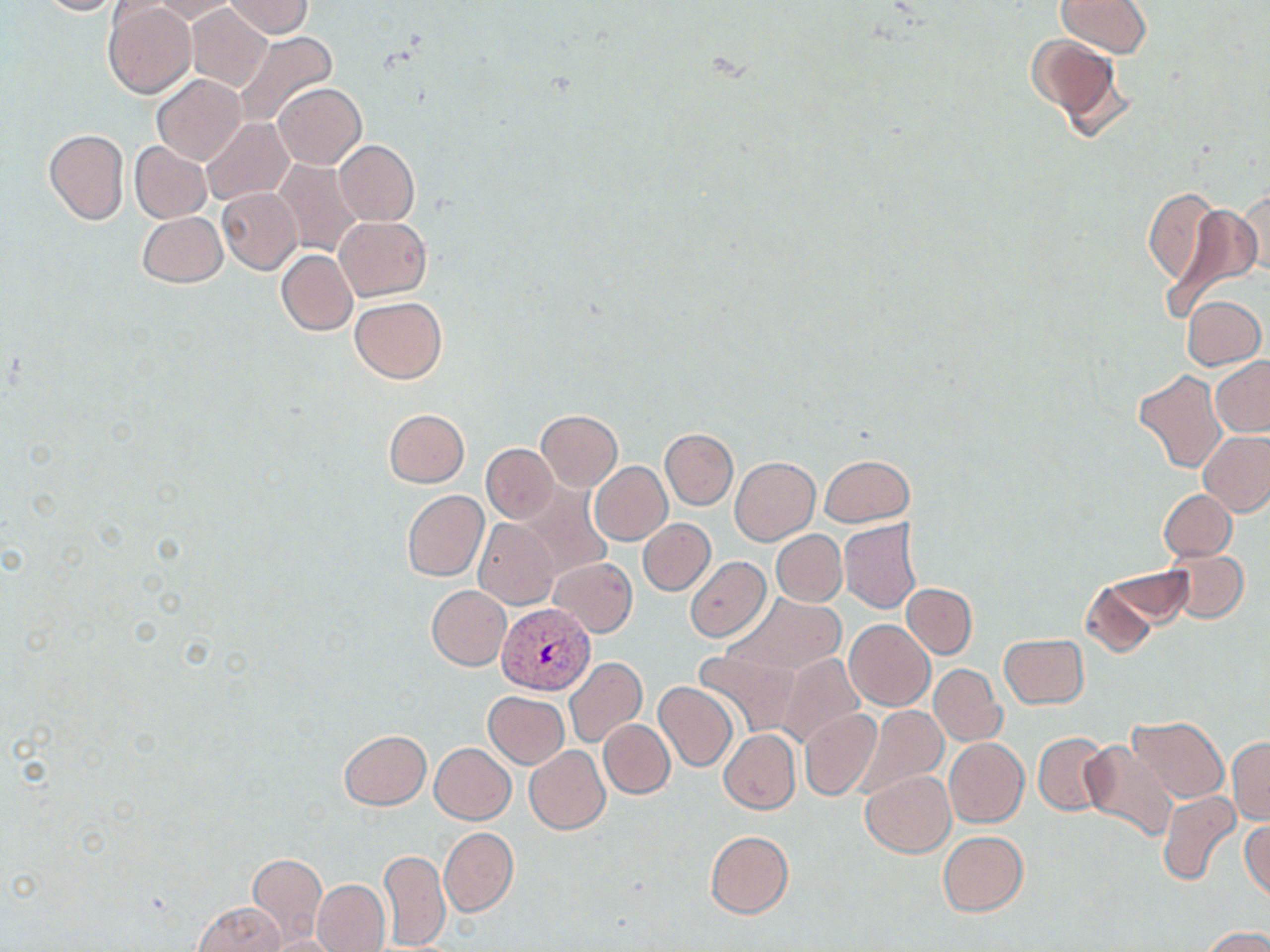
Summary:
  - Coordinate format: approximate bounding boxes as (x1,y1)-(x2,y2) corner pairs in pixels
  - Uninfected red blood cell locations: (35,0)-(132,16), (224,0)-(312,39), (1057,0)-(1153,57), (149,1)-(238,22), (105,3)-(196,98), (185,4)-(272,92), (206,4)-(308,66), (234,31)-(337,129), (1026,33)-(1128,135), (153,75)-(245,164), (274,83)-(366,168), (201,119)-(294,205), (43,129)-(129,226), (334,139)-(419,226), (130,141)-(211,222), (273,157)-(365,259), (1143,187)-(1220,289), (218,188)-(303,273), (1237,190)-(1269,278), (1160,203)-(1262,318), (137,211)-(227,287), (334,215)-(431,301), (276,250)-(358,335), (1182,295)-(1266,371), (350,296)-(447,383), (1212,358)-(1270,437), (1134,369)-(1226,473), (384,408)-(469,487), (537,409)-(622,492), (660,429)-(738,509), (1198,431)-(1270,515), (482,443)-(557,523), (820,454)-(913,526), (730,457)-(819,544), (588,461)-(672,546), (518,482)-(614,579), (1159,489)-(1237,561), (402,490)-(489,582), (639,518)-(715,595), (475,519)-(560,610), (838,519)-(923,614), (772,530)-(846,606), (1161,546)-(1249,624), (684,556)-(771,642), (549,558)-(637,636), (1104,567)-(1194,628), (1081,579)-(1160,656), (902,584)-(977,658), (426,585)-(511,670), (867,592)-(971,690), (727,593)-(847,675), (712,600)-(849,741), (845,621)-(934,711), (999,633)-(1089,709), (694,648)-(799,736), (775,653)-(866,748), (563,656)-(646,748), (930,663)-(1006,746), (654,682)-(737,771), (484,691)-(569,768), (854,703)-(948,797), (800,708)-(882,801), (1129,716)-(1229,802), (599,719)-(675,797), (339,729)-(431,810), (718,729)-(800,814), (1033,733)-(1111,817), (944,737)-(1028,827), (1228,737)-(1270,825), (1078,741)-(1179,843), (430,743)-(515,824), (524,745)-(609,834), (862,770)-(955,856), (1156,790)-(1240,887), (1241,818)-(1269,904), (439,828)-(517,916), (705,830)-(794,919), (938,831)-(1029,916), (379,849)-(450,948), (248,853)-(327,944), (312,879)-(389,952), (192,901)-(287,952), (1202,927)-(1270,952), (263,935)-(343,952)
  - Plasmodium vivax-infected red blood cell locations: (497,604)-(595,694)
  - Slide-level diagnosis: Plasmodium vivax
  - Field of view: one of a larger specimen
  - Image size: 1270×952 pixels
  - Magnification: 1000x
  - Stain: May-Grünwald-Giemsa
  - Modality: optical microscopy
  - Preparation: thin blood smear